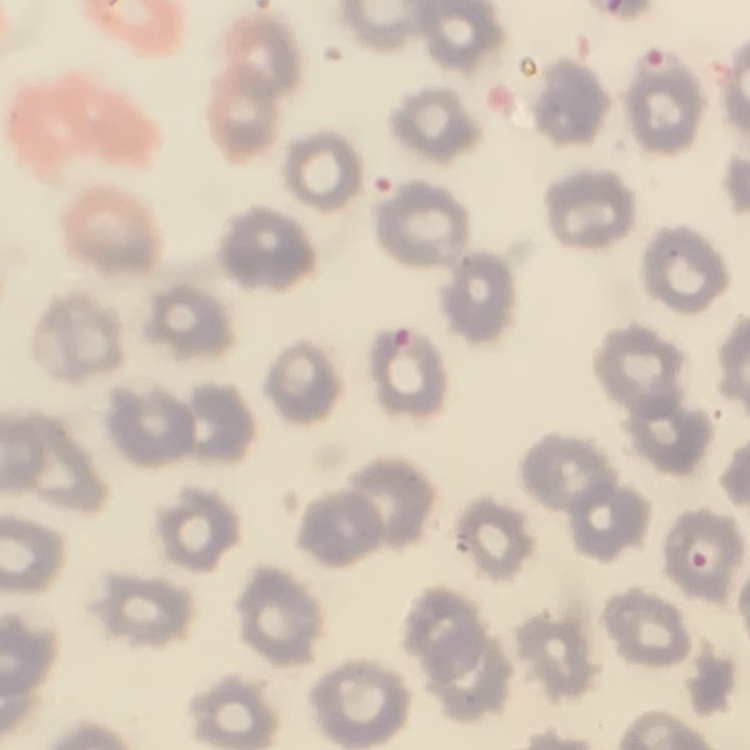
The erythrocytes exhibit no rouleaux formation. Stained with either Field's or Giemsa. One tile cut from a larger photomicrograph. Thin peripheral smear.